Comment on the morphology of the erythrocytes.
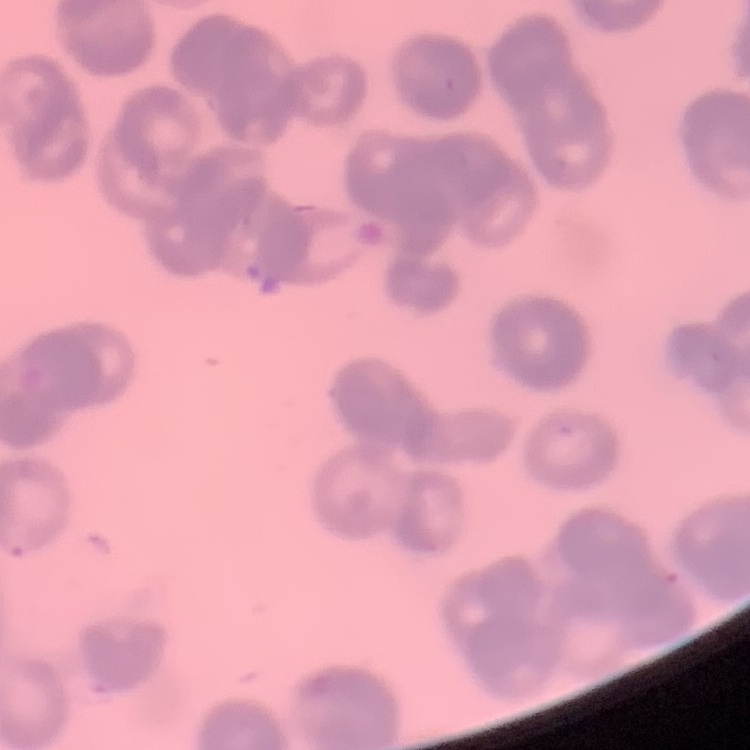
They show rouleaux formation.

Field's or Giemsa stain. Thin blood smear. Square crop of a larger photomicrograph.